Identify the blood parasite species.
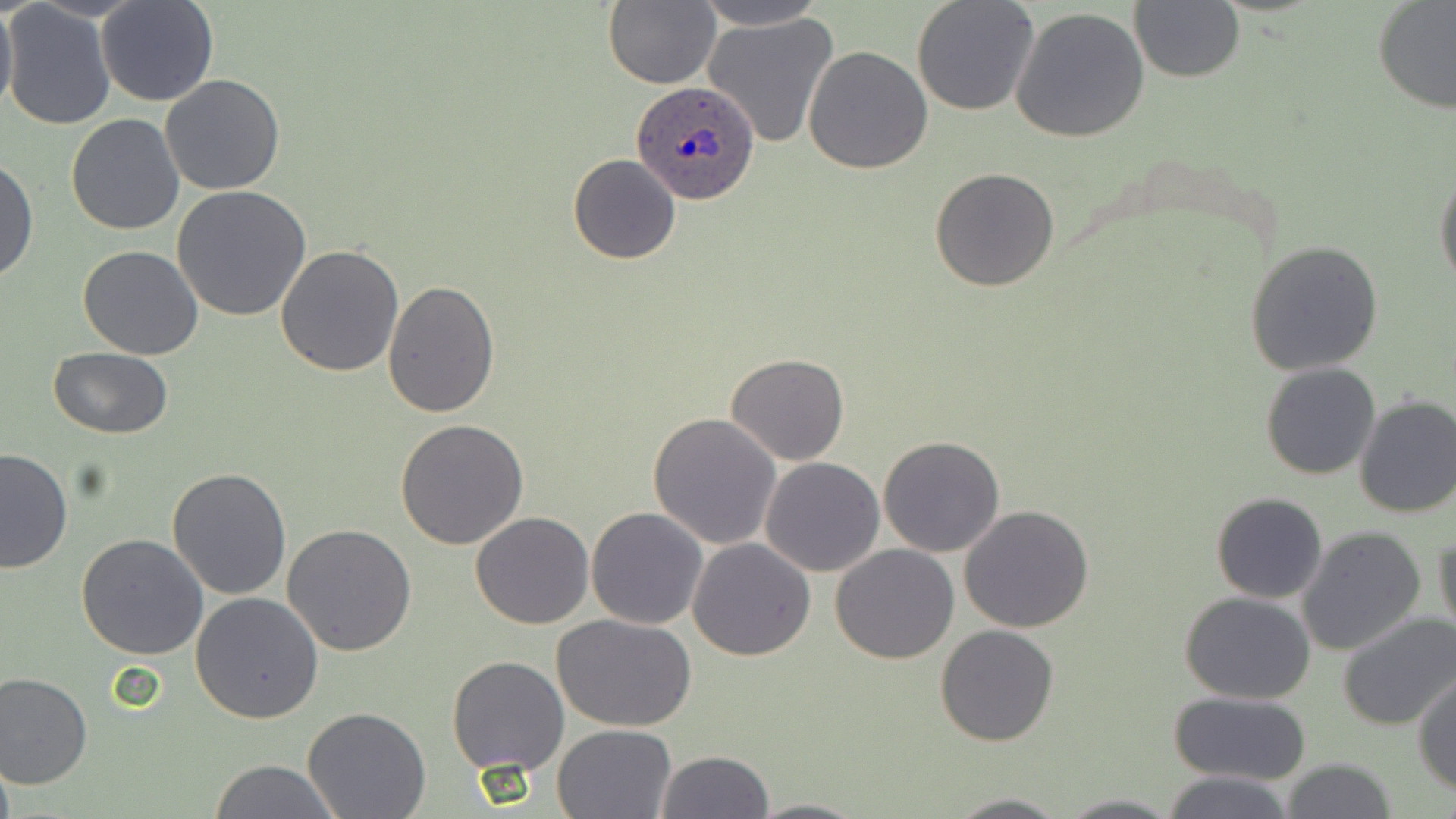
Plasmodium ovale.

Approximate bounding boxes as (x1,y1)-(x2,y2) corner pairs in pixels. Uninfected red blood cell locations: (96,0)-(217,106), (604,0)-(720,89), (692,0)-(827,30), (911,0)-(1039,116), (1372,1)-(1456,113), (0,2)-(18,119), (1129,2)-(1245,82), (2,4)-(117,132), (1009,6)-(1152,143), (700,11)-(840,151), (803,46)-(933,174), (160,74)-(285,195), (66,113)-(185,236), (567,154)-(680,264), (0,155)-(38,283), (930,168)-(1060,292), (1434,170)-(1455,292), (173,185)-(312,322), (1244,240)-(1386,376), (275,244)-(404,377), (77,245)-(204,361), (382,281)-(500,418), (48,346)-(173,440), (725,353)-(849,465), (1260,362)-(1380,480), (1353,395)-(1456,520), (647,412)-(782,550), (395,419)-(529,549), (879,435)-(1005,556), (0,447)-(75,575), (759,457)-(885,576), (167,466)-(293,599), (1211,492)-(1327,604), (959,505)-(1094,632), (587,507)-(708,629), (470,511)-(594,629), (282,523)-(416,654), (1296,526)-(1426,656), (1433,526)-(1455,643), (75,533)-(209,661), (688,537)-(816,660), (830,545)-(959,663), (190,592)-(324,723), (1179,592)-(1317,705), (1335,612)-(1456,731), (554,615)-(698,732), (935,625)-(1060,746), (445,655)-(569,776), (0,671)-(93,789), (1412,671)-(1456,795), (1169,691)-(1313,785), (303,707)-(432,819), (552,723)-(677,817), (654,750)-(775,818), (206,758)-(343,818), (1279,758)-(1398,818), (1161,771)-(1292,819), (940,793)-(1074,818), (1057,793)-(1182,818), (747,797)-(871,818). Plasmodium ovale-infected red blood cell locations: (633,80)-(760,206). May-Grünwald-Giemsa-stained preparation. Thin blood film. Image is 1456×819 pixels. 1000x magnification. Optical microscopy. One field of a larger specimen.